Report the malaria status of this cell.
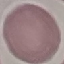
It is uninfected.

stain: Giemsa
capture: smartphone camera at the microscope eyepiece
image_type: cell patch, automatically extracted from a larger field of view and resized to 64 × 64 pixels
preparation: thin blood film